State which parasite is depicted.
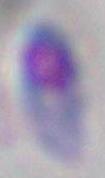

Toxoplasma gondii.

Micrograph. Captured at 1000x magnification.